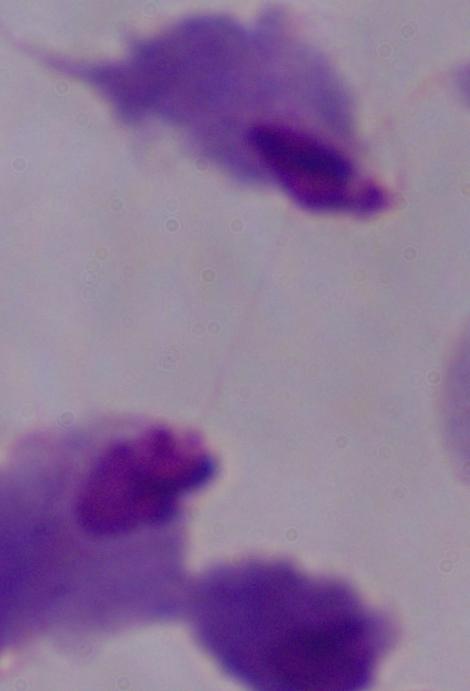
{
  "identification": "trichomonad",
  "magnification": "1000x",
  "modality": "micrograph"
}